Assess this cell for malaria.
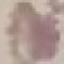

It is uninfected.

Automatically extracted cell patch, resized to 64 × 64 pixels. Photographed with a smartphone camera at the microscope eyepiece. Thin smear of blood. Giemsa-stained preparation.